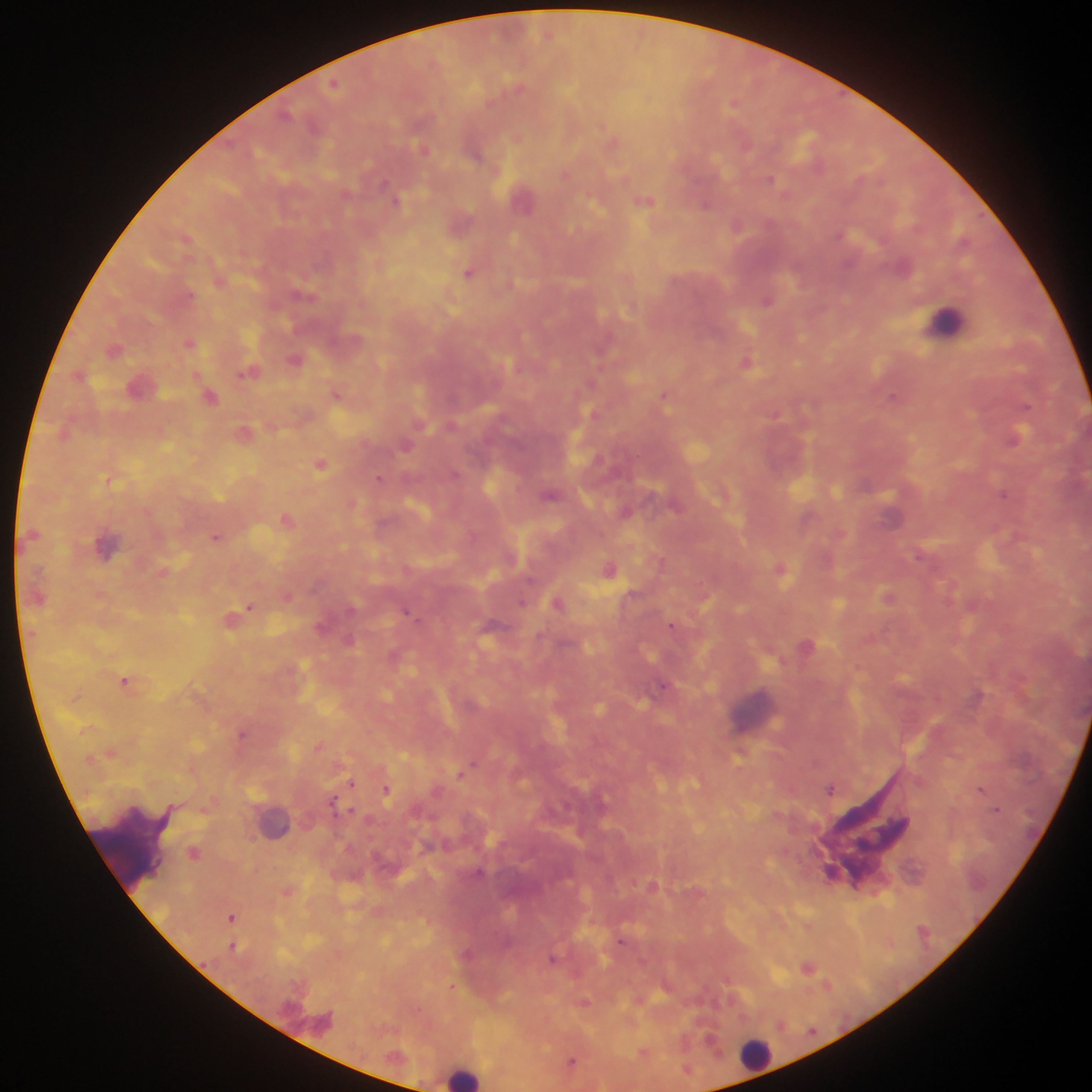

{
  "capture": "mobile-phone photograph through a microscope",
  "image_size": "1092×1092 pixels",
  "country": "Ghana",
  "malaria_parasite_locations": "approximate centers as [x, y] in pixels: [335, 83], [384, 183], [346, 193], [647, 201], [706, 204], [469, 272], [191, 296], [187, 342], [295, 360], [746, 362], [195, 371], [248, 372], [337, 392], [664, 394], [894, 396], [1027, 406], [1018, 436], [406, 446], [322, 463], [379, 477], [109, 482], [1004, 494], [215, 537], [660, 560], [782, 568], [888, 593], [98, 595], [288, 595], [250, 606], [407, 613], [672, 623], [126, 679], [663, 685], [242, 733], [319, 745], [474, 763], [459, 774], [351, 783], [982, 788], [387, 789], [830, 789], [333, 799], [353, 809], [997, 809], [205, 810], [195, 852], [233, 918], [621, 942], [233, 945], [554, 958], [809, 967], [728, 979], [827, 986], [452, 987], [573, 1059]",
  "leukocyte_locations": "approximate centers as [x, y] in pixels: [947, 323], [748, 1060], [461, 1076]",
  "field_of_view": "single",
  "preparation": "thick blood film"
}